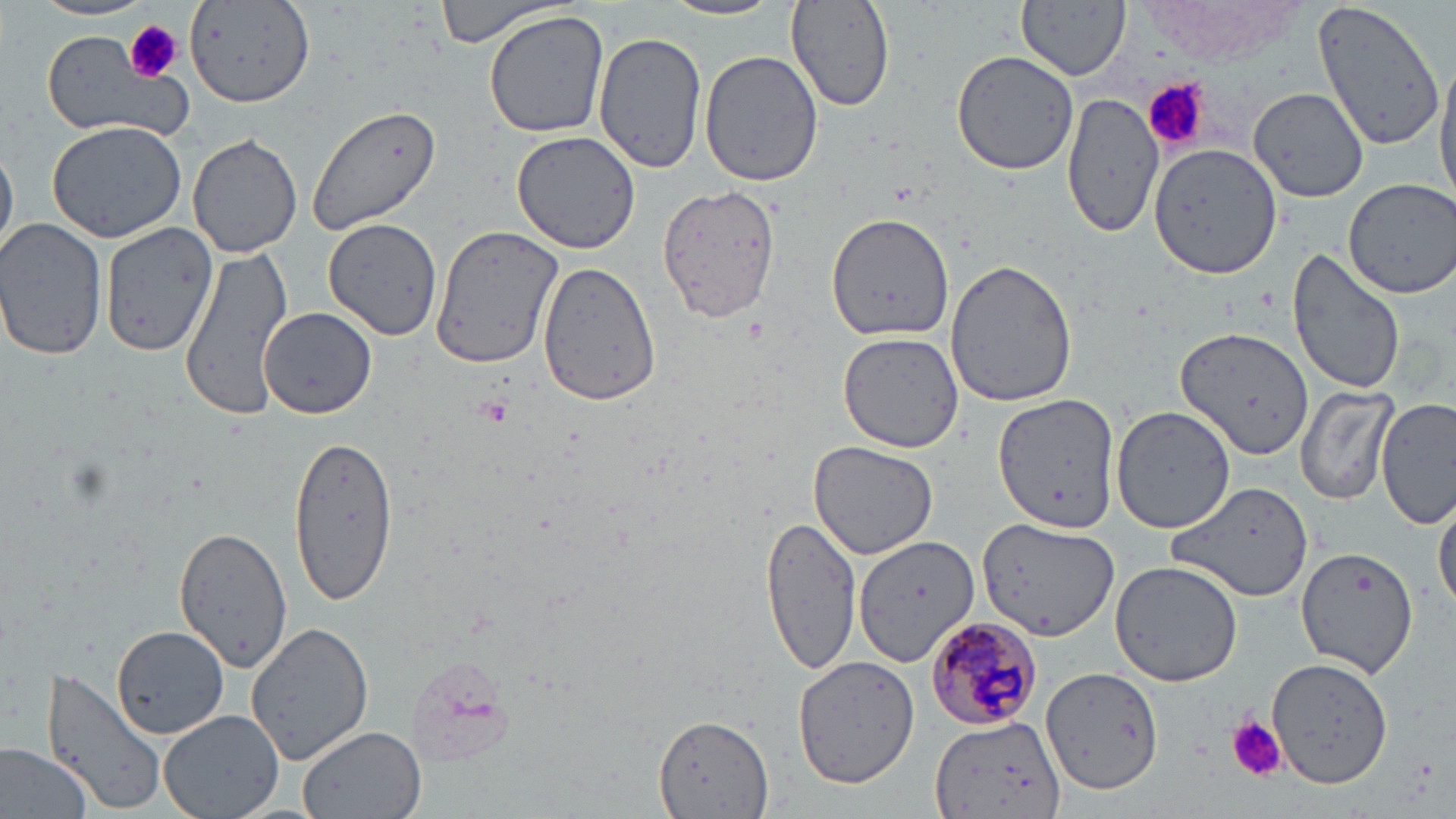
Summary:
  - Coordinate format: approximate bounding boxes as [x1, y1, x2, y2] in pixels
  - Plasmodium malariae-infected red blood cell locations: [922, 615, 1041, 734]
  - Platelet locations: [125, 22, 181, 83], [1144, 78, 1208, 153], [473, 396, 513, 429], [1226, 716, 1287, 782]
  - Uninfected red blood cell locations: [28, 0, 159, 22], [434, 0, 568, 49], [659, 0, 784, 22], [1019, 0, 1131, 81], [1311, 0, 1446, 153], [785, 1, 895, 111], [185, 3, 316, 108], [483, 10, 612, 138], [40, 29, 188, 143], [594, 30, 707, 176], [951, 49, 1079, 175], [699, 50, 823, 187], [1435, 57, 1456, 206], [1248, 86, 1369, 203], [1063, 91, 1166, 239], [305, 101, 445, 234], [46, 118, 189, 244], [512, 130, 640, 253], [188, 134, 303, 259], [0, 144, 17, 261], [1149, 145, 1283, 281], [1340, 178, 1456, 298], [656, 182, 781, 325], [827, 212, 956, 341], [0, 217, 107, 361], [325, 217, 444, 340], [99, 220, 215, 356], [431, 227, 561, 371], [178, 247, 294, 417], [1287, 247, 1406, 398], [537, 259, 663, 407], [945, 259, 1078, 409], [259, 306, 377, 419], [1178, 327, 1316, 462], [837, 330, 963, 455], [1295, 382, 1398, 507], [996, 395, 1122, 528], [1377, 395, 1455, 529], [1110, 404, 1238, 538], [284, 433, 401, 606], [808, 443, 938, 559], [1171, 481, 1315, 604], [1435, 494, 1455, 618], [761, 517, 862, 677], [977, 517, 1119, 644], [173, 527, 294, 672], [855, 536, 980, 663], [1296, 546, 1420, 679], [1109, 560, 1244, 685], [247, 621, 375, 765], [113, 623, 224, 746], [793, 651, 919, 790], [1269, 655, 1394, 788], [1040, 665, 1166, 793], [43, 668, 166, 815], [158, 709, 284, 819], [927, 715, 1069, 818], [654, 716, 774, 819], [299, 725, 426, 819], [0, 739, 98, 819]
  - Slide-level diagnosis: Plasmodium malariae
  - Stain: May-Grünwald-Giemsa
  - Preparation: thin blood film
  - Magnification: 1000x
  - Modality: optical microscopy
  - Field of view: one of a larger specimen
  - Image size: 1456×819 pixels